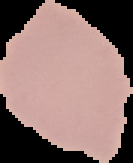

Summary:
  - Preparation: thin blood smear
  - Result: negative for Plasmodium parasites
  - Image size: 133×163 pixels
  - Image type: segmented cell region on a black background